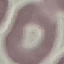
Malaria status: uninfected. Giemsa-stained preparation. Automatically extracted cell patch, resized to 64 × 64 pixels. Thin blood film. Acquired by smartphone through the microscope eyepiece.